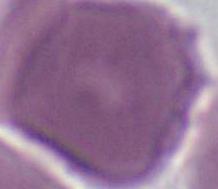

Summary:
  - Modality: photomicrograph
  - Identification: red blood cell
  - Magnification: 1000x